Assess this cell for malaria.
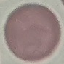
Uninfected.

Automatically extracted cell patch, resized to 64 × 64 pixels. Photographed with a smartphone camera at the microscope eyepiece. Thin blood smear. Giemsa-stained preparation.